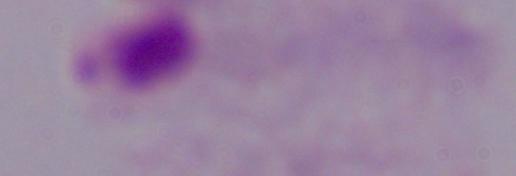

Summary:
  - Identification: trichomonad
  - Modality: photomicrograph
  - Magnification: 1000x